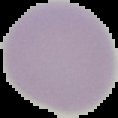
image type = segmented cell region on a black background
preparation = thin blood smear
result = no Plasmodium parasites detected
image size = 118×118 pixels